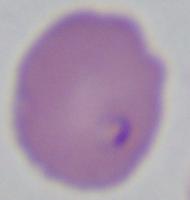 Micrograph. 1000x magnification. A Babesia parasite is shown.